Locate every uninfected red blood cell.
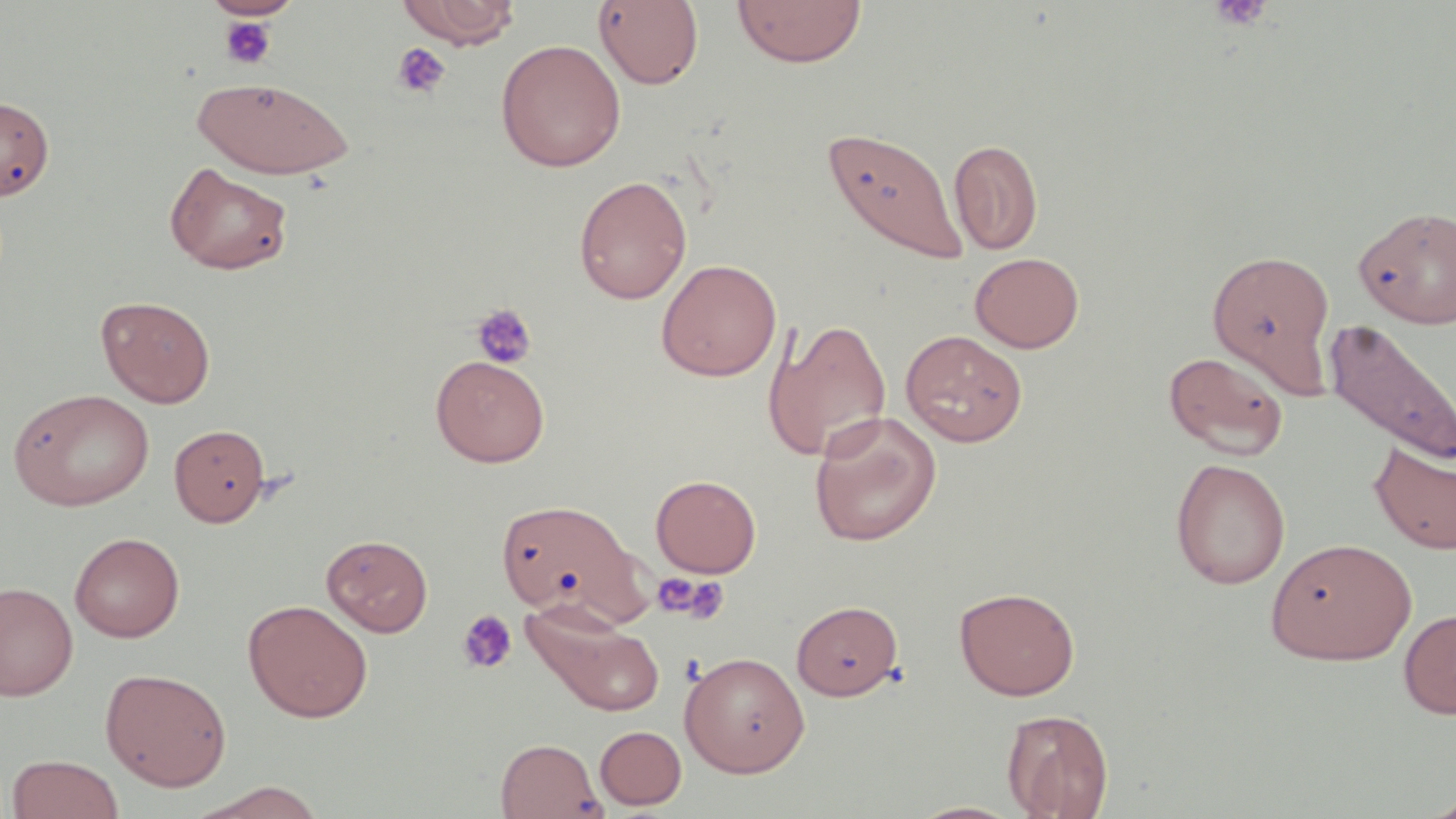

Approximate bounding boxes as (x1,y1)-(x2,y2) corner pairs in pixels.
Uninfected red blood cells: (205,0)-(302,19), (397,0)-(520,48), (732,0)-(866,68), (593,1)-(705,90), (495,39)-(627,172), (191,76)-(354,179), (0,96)-(54,200), (823,125)-(968,267), (949,138)-(1043,254), (164,161)-(294,275), (573,175)-(692,304), (1354,204)-(1456,328), (1208,247)-(1336,393), (970,252)-(1084,353), (656,258)-(782,381), (96,295)-(216,407), (1324,316)-(1455,467), (763,317)-(892,463), (900,329)-(1028,447), (1162,350)-(1289,461), (431,355)-(550,467), (7,388)-(155,511), (809,411)-(942,546), (169,424)-(271,527), (1369,442)-(1456,555), (1170,457)-(1290,589), (651,474)-(761,577), (494,491)-(648,628), (69,532)-(185,642), (321,534)-(434,636), (1266,537)-(1417,665), (1,581)-(78,701), (954,586)-(1080,700), (243,599)-(373,723), (791,599)-(903,700), (520,603)-(668,718), (1398,608)-(1456,719), (679,651)-(810,777), (99,666)-(232,791), (1001,708)-(1113,818), (594,725)-(687,810), (495,737)-(605,819), (6,754)-(123,819), (186,781)-(329,818), (1417,793)-(1456,819), (904,800)-(1027,819).

Platelet locations: (1208,0)-(1273,31), (219,15)-(277,70), (391,42)-(451,98), (471,303)-(537,369), (653,573)-(729,624), (457,609)-(518,674). Slide-level diagnosis: no evidence of blood parasites. One field of a larger specimen. Optical microscopy. 1000x magnification. May-Grünwald-Giemsa-stained preparation. Thin blood film. Image is 1456×819 pixels.